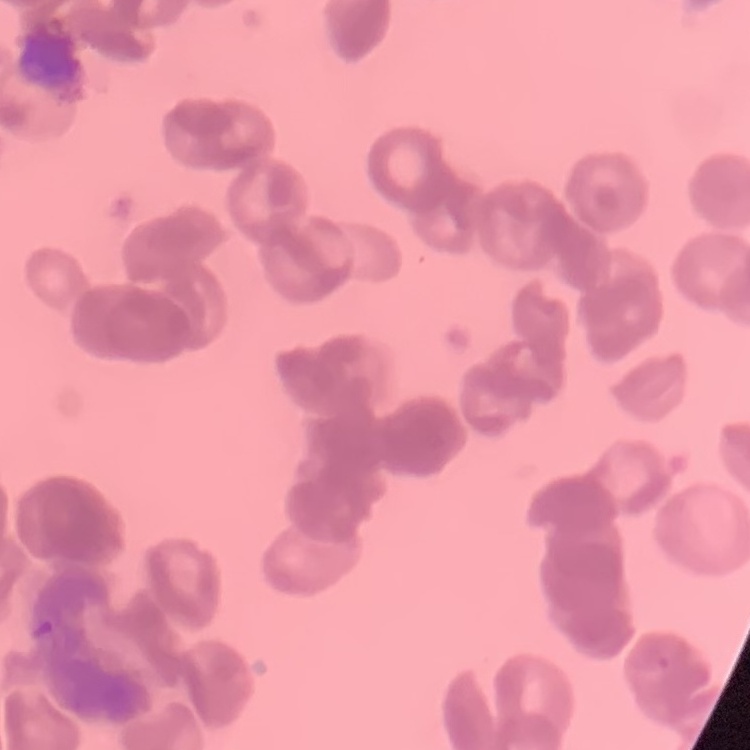

red blood cell morphology = rouleaux formation
preparation = thin peripheral smear
image type = square crop of a larger photomicrograph
stain = Field's or Giemsa